Identify the parasite.
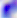
This is Toxoplasma gondii.

Captured at 400x magnification. Photomicrograph.